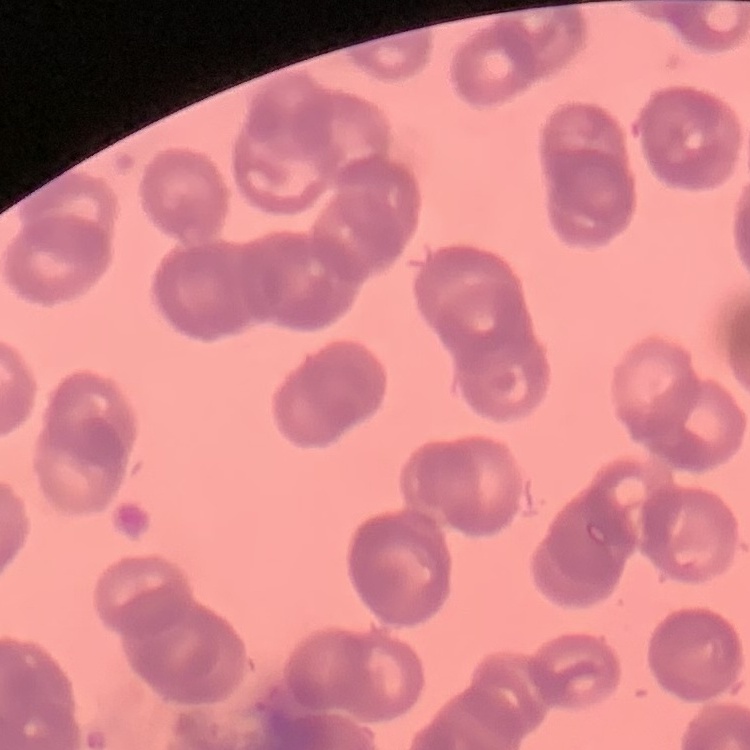
The erythrocytes show rouleaux formation. Thin blood film. Field's or Giemsa stain. One tile cut from a larger photomicrograph.